Assess this cell for malaria.
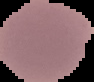

Uninfected.

From a thin blood smear. Image is 94×82 pixels. Cell region segmented out of the field of view; the surrounding area is masked to black.